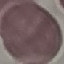
Malaria status: uninfected. Giemsa-stained preparation. Acquired by smartphone through the microscope eyepiece. Automatically extracted cell patch, resized to 64 × 64 pixels. Thin blood film.